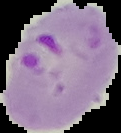

Summary:
  - Preparation: thin blood smear
  - Image size: 121×133 pixels
  - Result: malaria parasites detected
  - Image type: segmented cell region with the area outside set to black